Comment on the morphology of the red blood cells.
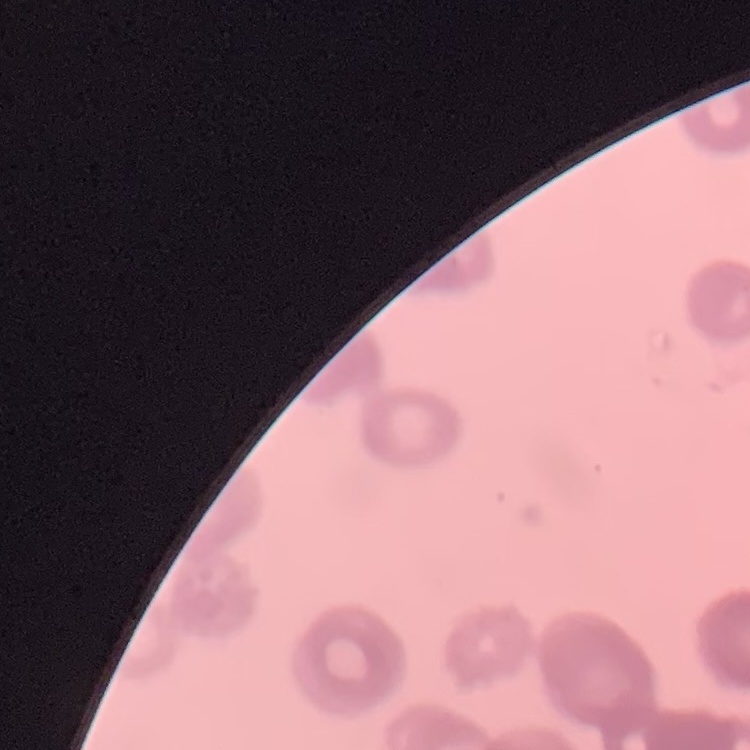
They show rouleaux formation.

Summary:
  - Preparation: thin blood smear
  - Image type: square crop of a larger photomicrograph
  - Stain: Field's or Giemsa